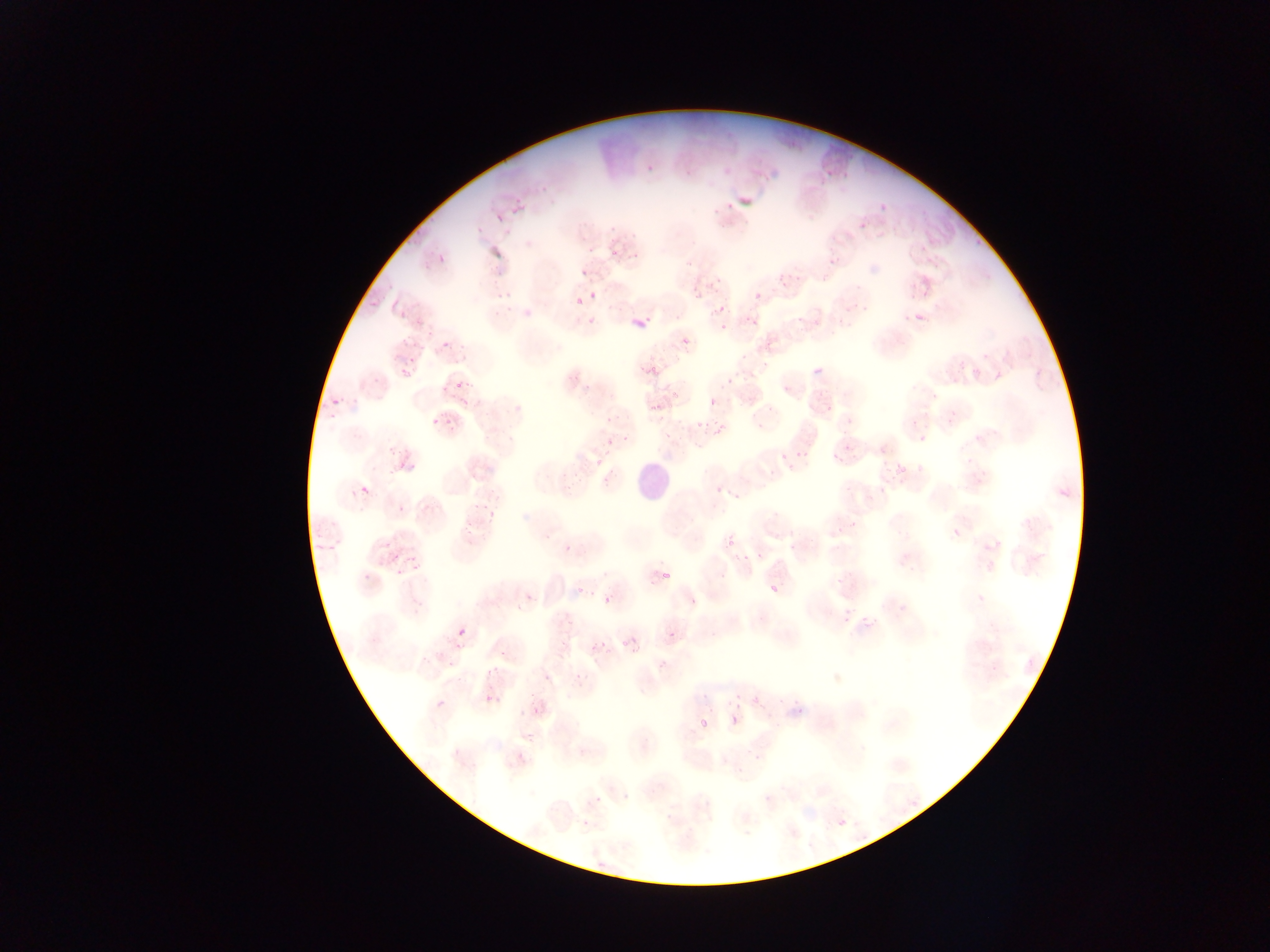
capture: mobile-phone photograph through a microscope
leukocyte_locations: 'approximate bounding boxes as {left, top, right, bottom} in pixels: {632, 461, 675, 507}'
image_size: 1270×952 pixels
plasmodium_parasite_locations: 'approximate bounding boxes as {left, top, right, bottom} in pixels: {510, 197, 519, 218}, {877, 201, 888, 209}, {858, 210, 872, 228}, {494, 214, 506, 227}, {916, 239, 933, 253}, {623, 242, 643, 261}, {610, 248, 619, 256}, {438, 250, 451, 262}, {682, 256, 695, 267}, {578, 267, 588, 275}, {778, 267, 801, 286}, {906, 272, 922, 293}, {712, 275, 725, 287}, {496, 286, 513, 298}, {369, 290, 386, 308}, {589, 291, 597, 300}, {754, 292, 762, 301}, {716, 297, 730, 308}, {572, 300, 583, 308}, {912, 304, 931, 323}, {628, 305, 656, 326}, {835, 307, 847, 323}, {399, 308, 413, 320}, {585, 312, 602, 322}, {744, 312, 765, 324}, {718, 322, 728, 329}, {429, 324, 442, 335}, {680, 336, 692, 349}, {438, 339, 456, 355}, {736, 349, 748, 360}, {405, 354, 419, 367}, {816, 362, 826, 375}, {647, 363, 661, 376}, {394, 367, 408, 377}, {723, 368, 742, 385}, {454, 376, 465, 391}, {440, 383, 448, 394}, {459, 389, 472, 405}, {665, 391, 678, 405}, {644, 398, 663, 412}, {708, 398, 718, 408}, {821, 398, 838, 411}, {330, 401, 343, 409}, {447, 408, 455, 431}, {429, 409, 443, 429}, {330, 412, 342, 424}, {698, 419, 701, 429}, {916, 420, 931, 438}, {710, 423, 727, 436}, {352, 426, 366, 438}, {828, 426, 854, 460}, {661, 431, 672, 439}, {388, 440, 402, 457}, {601, 440, 613, 448}, {794, 450, 807, 467}, {597, 453, 607, 462}, {402, 455, 412, 465}, {777, 455, 788, 462}, {786, 460, 797, 469}, {916, 465, 925, 471}, {887, 466, 901, 485}, {560, 472, 577, 494}, {597, 472, 610, 488}, {710, 481, 731, 494}, {358, 484, 370, 497}, {472, 500, 478, 512}, {393, 503, 409, 516}, {485, 503, 501, 518}, {462, 514, 473, 537}, {839, 518, 848, 529}, {727, 523, 743, 542}, {949, 526, 963, 541}, {383, 534, 396, 550}, {562, 541, 577, 552}, {785, 542, 799, 550}, {393, 552, 401, 563}, {410, 553, 421, 569}, {736, 553, 749, 561}, {395, 564, 403, 574}, {363, 567, 377, 583}, {660, 570, 672, 583}, {575, 572, 592, 595}, {832, 573, 847, 586}, {769, 582, 783, 598}, {521, 584, 533, 602}, {512, 595, 521, 607}, {604, 595, 614, 606}, {858, 605, 883, 637}, {565, 617, 574, 627}, {618, 625, 638, 647}, {457, 627, 467, 638}, {666, 630, 677, 642}, {600, 637, 616, 654}, {585, 640, 597, 650}, {439, 649, 456, 664}, {632, 649, 638, 660}, {1024, 655, 1040, 674}, {482, 657, 503, 673}, {652, 661, 660, 672}, {540, 665, 555, 681}, {572, 673, 581, 690}, {701, 687, 715, 705}, {750, 687, 764, 705}, {721, 691, 741, 705}, {485, 694, 496, 704}, {526, 694, 548, 712}, {435, 699, 446, 711}, {789, 700, 803, 717}, {729, 714, 741, 728}, {699, 718, 710, 730}, {521, 728, 538, 748}, {594, 792, 607, 803}, {623, 796, 634, 804}, {835, 816, 848, 830}, {581, 819, 591, 829} | approximate {x, y} pixel centers of objects too small to bound: {727, 205}, {783, 392}, {844, 625}'
country: Ghana
field_of_view: single
preparation: thin blood film